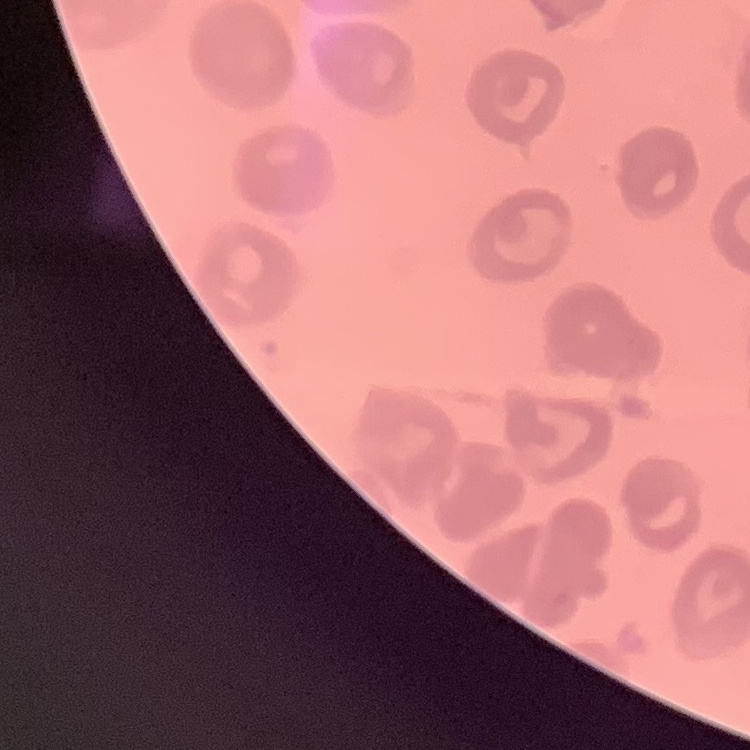
red blood cell morphology = no rouleaux formation
preparation = thin blood film
stain = Field's or Giemsa
image type = square crop of a larger photomicrograph